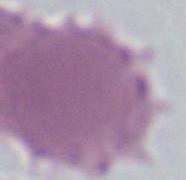
identification: erythrocyte
modality: micrograph
magnification: 1000x